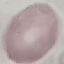

Summary:
  - Result: no malaria parasites detected
  - Preparation: thin blood smear
  - Capture: smartphone camera at the microscope eyepiece
  - Image type: automatically extracted cell patch, resized to 64 × 64 pixels
  - Stain: Giemsa